Assess the morphology of the red blood cells.
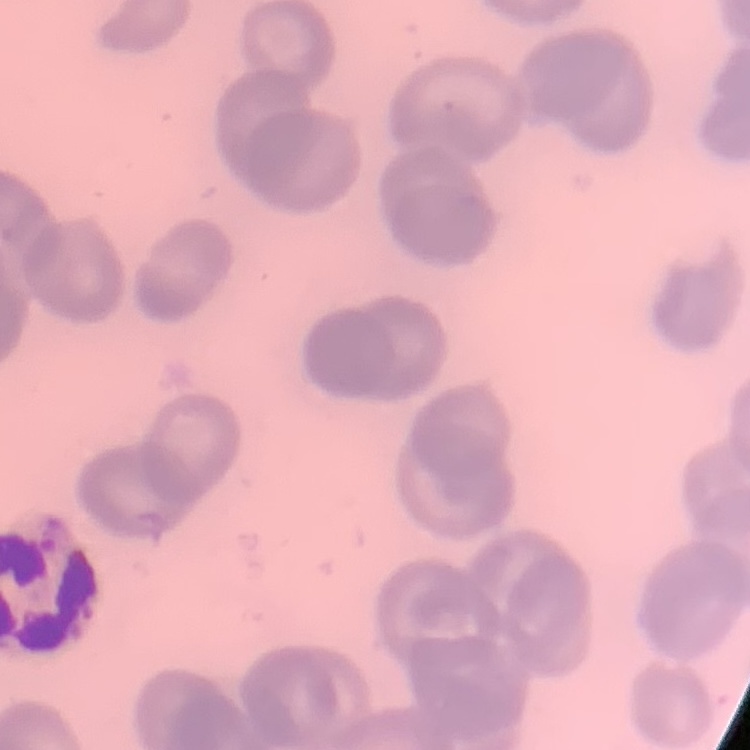

They show no rouleaux formation.

Field's or Giemsa stain. Square crop of a larger photomicrograph. Thin blood film.